Classify this cell by malaria status.
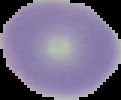
Uninfected.

image size = 121×100 pixels
image type = segmented cell region on a black background
preparation = thin blood smear